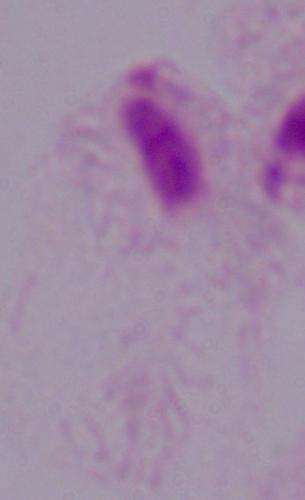

Micrograph. Captured at 1000x magnification. A trichomonad is seen.